Identify the cell.
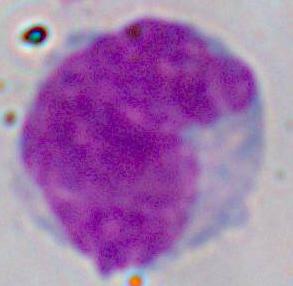

This is a leukocyte.

Micrograph. Captured at 1000x magnification.